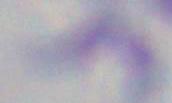

identification = Toxoplasma gondii
modality = micrograph
magnification = 1000x